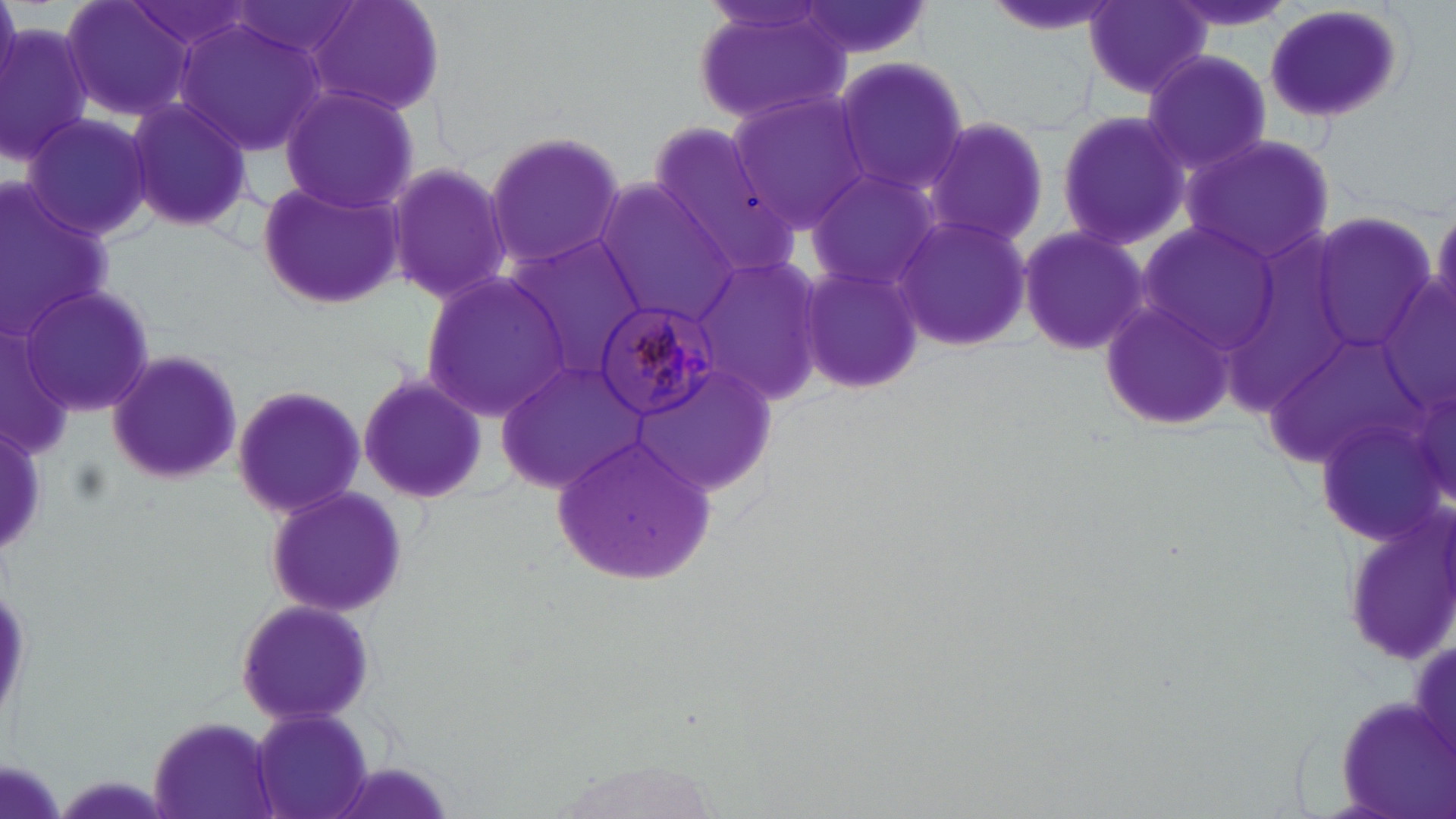
Approximate bounding boxes as [x1, y1, x2, y2] in pixels. Uninfected red blood cell locations: [59, 0, 198, 124], [308, 0, 447, 117], [686, 0, 853, 129], [793, 0, 937, 64], [1083, 0, 1212, 99], [1159, 0, 1298, 37], [1262, 4, 1410, 122], [178, 18, 324, 154], [1, 19, 96, 167], [1143, 49, 1273, 182], [832, 55, 969, 199], [277, 85, 420, 212], [725, 88, 875, 233], [122, 96, 256, 236], [1053, 106, 1189, 255], [22, 110, 157, 245], [925, 116, 1051, 249], [642, 124, 800, 282], [482, 128, 628, 275], [1183, 135, 1333, 267], [381, 158, 515, 307], [805, 163, 948, 296], [0, 177, 114, 338], [255, 177, 407, 312], [593, 180, 739, 323], [1428, 205, 1456, 327], [891, 213, 1032, 354], [1307, 216, 1442, 357], [1136, 222, 1282, 353], [1015, 224, 1148, 358], [501, 234, 650, 383], [693, 254, 830, 402], [795, 260, 927, 397], [418, 271, 571, 416], [18, 282, 153, 417], [1096, 297, 1238, 433], [103, 349, 244, 488], [496, 357, 654, 495], [630, 357, 777, 499], [355, 369, 489, 507], [229, 384, 367, 519], [551, 434, 721, 586], [261, 485, 408, 620], [232, 597, 377, 727], [1330, 695, 1456, 819], [250, 707, 376, 819], [147, 715, 282, 819], [319, 758, 461, 819]. Plasmodium malariae-infected red blood cell locations: [591, 295, 722, 416]. Slide-level diagnosis: Plasmodium malariae. Optical microscopy. May-Grünwald-Giemsa stain. Thin blood smear. 1000x magnification. Single field of view. Image is 1456×819 pixels.